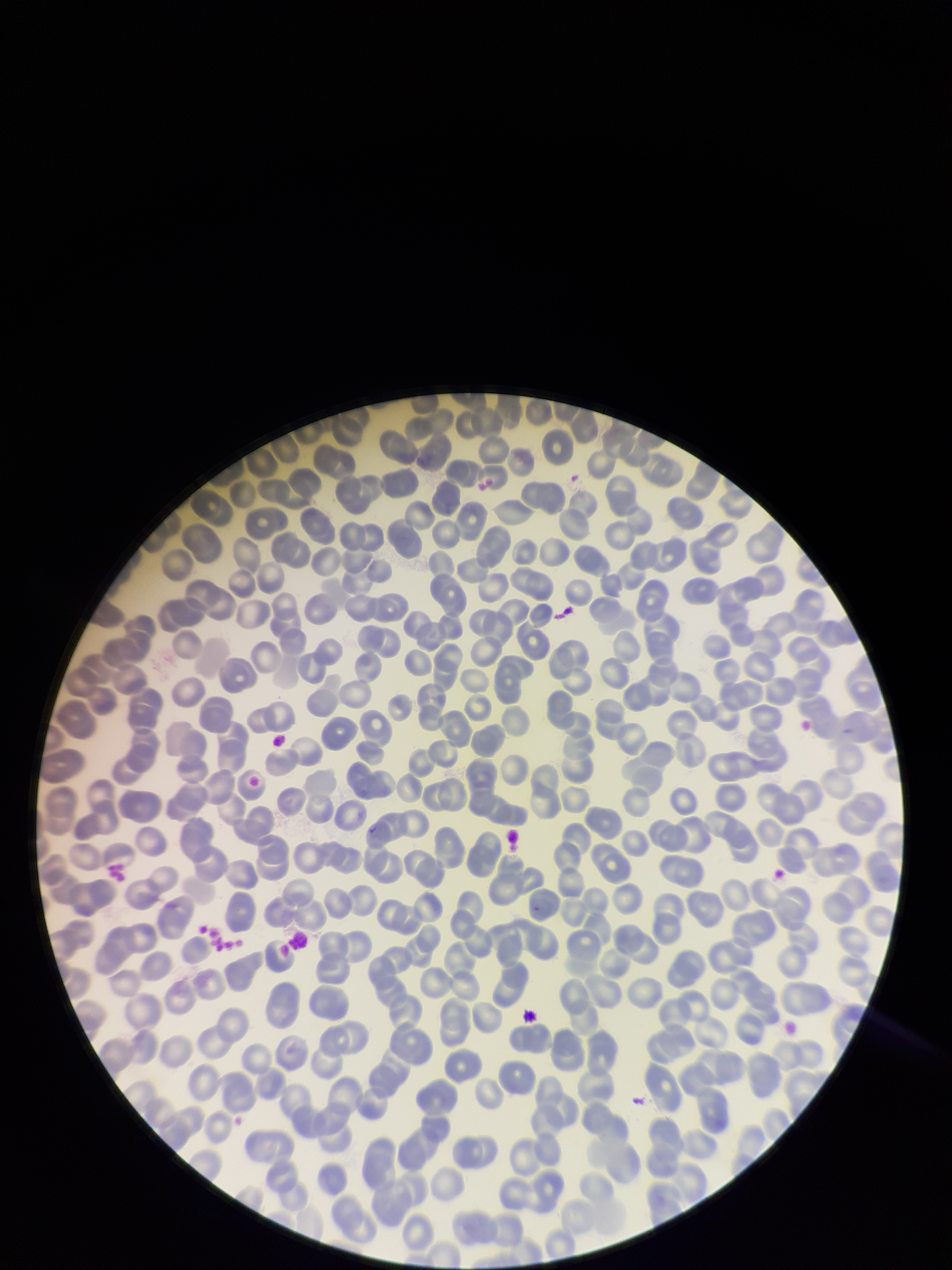

Red blood cell count: 284. Preparation: thin blood smear. Giemsa stain. Image is 952×1270 pixels. One field from this slide. Patient malaria status: negative. Parasitized red blood cell count: 0. Parasitized red blood cells: none identified. Smartphone photograph taken through the eyepiece of a microscope.